State which parasite is depicted.
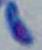

Toxoplasma gondii.

Photomicrograph. 1000x magnification.